Comment on the morphology of the red blood cells.
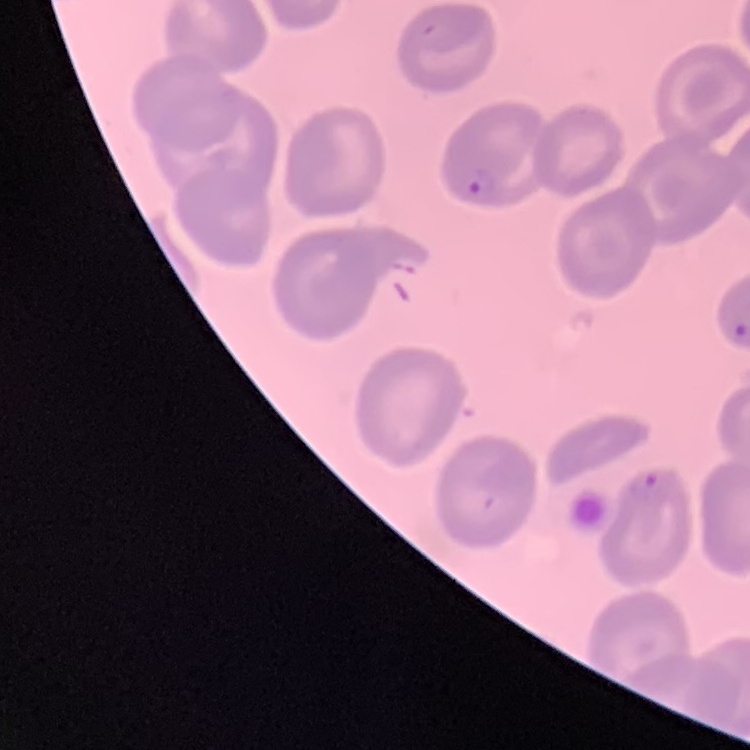
No rouleaux formation.

image_type: square crop of a larger photomicrograph
stain: Field's or Giemsa
preparation: thin blood smear